Locate every Plasmodium vivax-infected red blood cell.
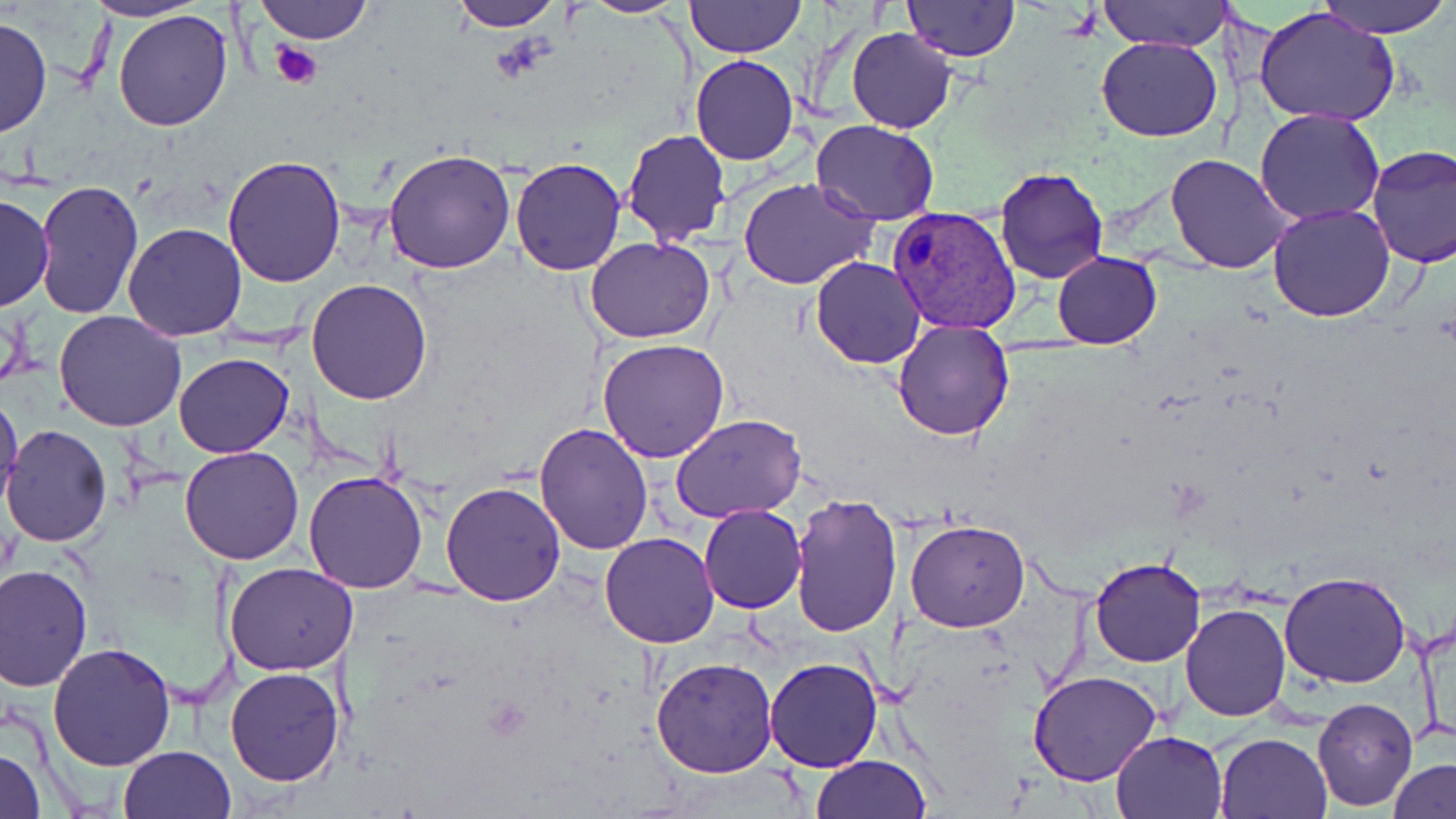

Approximate bounding boxes as (x1, y1, x2, y2) in pixels.
Plasmodium vivax-infected red blood cells: (888, 204, 1022, 334).

Summary:
  - Uninfected red blood cell locations: (87, 0, 203, 21), (448, 0, 561, 30), (576, 0, 688, 17), (685, 0, 804, 58), (901, 0, 1018, 62), (1314, 0, 1453, 38), (254, 1, 374, 44), (1097, 1, 1228, 52), (1254, 5, 1403, 127), (112, 9, 234, 130), (0, 16, 51, 140), (846, 27, 955, 133), (1096, 35, 1222, 142), (690, 54, 800, 165), (1254, 108, 1385, 225), (810, 118, 941, 225), (620, 130, 732, 247), (1367, 144, 1456, 267), (385, 149, 516, 274), (222, 154, 348, 287), (1165, 154, 1295, 274), (510, 156, 626, 275), (994, 165, 1108, 284), (736, 177, 881, 292), (32, 180, 144, 322), (0, 191, 52, 314), (1267, 203, 1395, 321), (123, 222, 248, 341), (585, 237, 715, 343), (1052, 252, 1162, 348), (811, 257, 925, 368), (306, 279, 432, 405), (53, 311, 186, 431), (893, 320, 1016, 439), (598, 339, 730, 464), (173, 353, 294, 457), (0, 387, 23, 518), (672, 414, 806, 525), (535, 423, 652, 556), (1, 424, 114, 547), (179, 446, 304, 565), (302, 469, 431, 593), (441, 481, 566, 604), (791, 493, 901, 636), (699, 505, 806, 615), (905, 520, 1029, 632), (600, 532, 719, 647), (1089, 556, 1205, 667), (224, 563, 361, 677), (1, 564, 93, 691), (1127, 569, 1257, 716), (1280, 571, 1411, 689), (1181, 602, 1292, 721), (1413, 614, 1453, 749), (47, 641, 177, 771), (651, 656, 777, 778), (764, 656, 884, 772), (225, 666, 345, 786), (1029, 671, 1162, 787), (1313, 697, 1418, 812), (1111, 730, 1230, 819), (1216, 731, 1332, 819), (120, 746, 236, 819), (1, 747, 46, 818), (812, 754, 930, 818), (1388, 758, 1456, 819)
  - Platelet locations: (270, 41, 324, 92)
  - Slide-level diagnosis: Plasmodium vivax
  - Stain: May-Grünwald-Giemsa
  - Field of view: single
  - Preparation: thin blood smear
  - Modality: optical microscopy
  - Magnification: 1000x
  - Image size: 1456×819 pixels